Identify the cell.
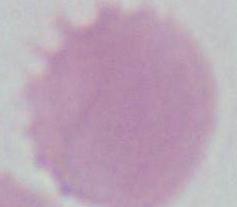
This is an erythrocyte.

Summary:
  - Magnification: 1000x
  - Modality: micrograph